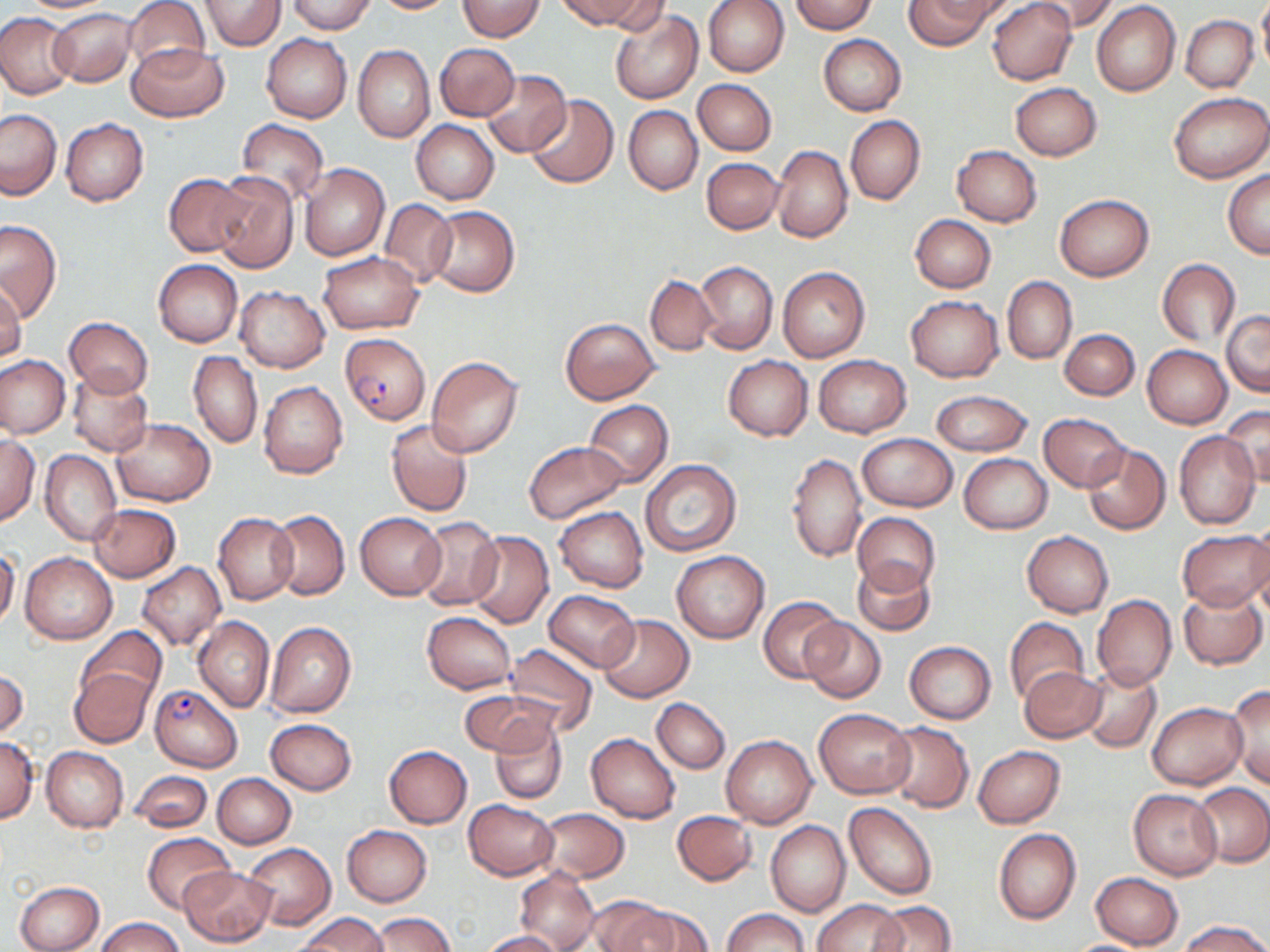

Summary:
  - Coordinate format: approximate bounding boxes as [x1, y1, x2, y2] in pixels
  - Uninfected red blood cell locations: [14, 0, 120, 14], [124, 0, 209, 75], [200, 0, 286, 50], [288, 0, 376, 34], [372, 0, 460, 14], [558, 0, 650, 31], [701, 0, 790, 78], [904, 0, 998, 51], [987, 0, 1077, 85], [1030, 0, 1120, 33], [1257, 0, 1270, 77], [458, 1, 543, 40], [601, 1, 670, 35], [790, 1, 877, 33], [1092, 2, 1181, 97], [51, 8, 136, 86], [609, 8, 704, 105], [0, 13, 76, 98], [1181, 16, 1258, 92], [261, 33, 351, 124], [818, 34, 906, 116], [127, 43, 228, 121], [435, 44, 519, 121], [353, 45, 434, 142], [482, 69, 571, 157], [693, 79, 776, 155], [1010, 82, 1102, 161], [1168, 92, 1269, 183], [527, 94, 618, 189], [624, 105, 702, 195], [0, 109, 62, 198], [845, 115, 925, 206], [60, 119, 148, 206], [235, 119, 329, 205], [411, 121, 499, 204], [772, 144, 852, 243], [951, 146, 1041, 226], [702, 157, 783, 234], [300, 164, 390, 260], [1223, 169, 1270, 258], [211, 171, 300, 274], [164, 174, 252, 257], [1054, 194, 1154, 281], [380, 198, 457, 287], [426, 206, 519, 296], [910, 215, 997, 292], [0, 220, 62, 321], [318, 251, 424, 334], [1157, 259, 1241, 346], [154, 260, 242, 347], [695, 260, 778, 355], [777, 267, 870, 361], [645, 275, 717, 355], [1003, 276, 1077, 364], [0, 285, 26, 362], [234, 286, 331, 372], [907, 296, 1003, 381], [1222, 311, 1270, 396], [64, 318, 153, 399], [560, 318, 660, 404], [1060, 328, 1140, 401], [1142, 345, 1232, 428], [188, 351, 262, 448], [0, 355, 70, 438], [723, 355, 813, 441], [813, 356, 910, 438], [427, 357, 523, 458], [67, 369, 153, 456], [258, 381, 348, 479], [930, 390, 1032, 456], [420, 397, 513, 504], [584, 401, 673, 486], [1220, 406, 1270, 486], [1038, 412, 1129, 491], [111, 418, 215, 507], [385, 418, 475, 517], [1174, 431, 1260, 530], [857, 434, 957, 511], [0, 437, 39, 525], [523, 439, 629, 524], [1081, 443, 1172, 534], [41, 450, 121, 545], [787, 452, 867, 562], [959, 454, 1051, 534], [641, 459, 742, 557], [88, 503, 181, 582], [555, 507, 648, 593], [270, 510, 349, 600], [355, 512, 446, 600], [853, 512, 941, 597], [213, 513, 299, 605], [415, 516, 504, 611], [1249, 517, 1270, 610], [1176, 530, 1269, 612], [466, 531, 554, 629], [1022, 531, 1114, 616], [0, 548, 19, 628], [672, 551, 769, 643], [21, 553, 117, 644], [853, 560, 934, 636], [137, 562, 226, 651], [1178, 587, 1268, 670], [545, 589, 639, 673], [1091, 594, 1177, 690], [760, 596, 843, 683], [422, 612, 515, 693], [599, 614, 694, 701], [193, 617, 274, 712], [800, 617, 886, 703], [1004, 617, 1089, 707], [266, 622, 357, 719], [78, 627, 167, 709], [905, 641, 996, 723], [503, 644, 599, 736], [1080, 663, 1162, 754], [1019, 666, 1107, 743], [69, 668, 154, 748], [0, 670, 28, 739], [1226, 685, 1269, 790], [461, 690, 554, 759], [652, 697, 730, 773], [1147, 701, 1246, 789], [814, 708, 915, 798], [265, 718, 358, 795], [490, 718, 566, 804], [881, 721, 974, 813], [586, 732, 681, 823], [722, 736, 816, 828], [0, 737, 40, 823], [41, 746, 128, 832], [384, 746, 472, 828], [973, 746, 1065, 827], [129, 771, 212, 833], [213, 773, 296, 848], [1192, 783, 1270, 867], [1129, 788, 1222, 880], [464, 799, 557, 879], [846, 803, 938, 900], [532, 807, 628, 883], [671, 810, 758, 886], [766, 821, 850, 918], [342, 824, 432, 906], [994, 829, 1080, 925], [143, 832, 233, 913], [243, 843, 336, 930], [178, 866, 277, 947], [515, 868, 600, 952], [1089, 871, 1185, 949], [14, 879, 104, 952], [584, 896, 673, 952], [814, 899, 906, 952], [869, 901, 957, 952], [611, 903, 710, 952], [723, 909, 807, 952], [373, 912, 453, 952], [299, 913, 388, 952], [95, 916, 184, 952], [1181, 920, 1269, 952], [480, 930, 563, 951], [1058, 938, 1158, 952]
  - Plasmodium falciparum-infected red blood cell locations: [340, 334, 430, 424], [150, 685, 242, 772]
  - Slide-level diagnosis: Plasmodium falciparum
  - Preparation: thin blood smear
  - Magnification: 1000x
  - Stain: May-Grünwald-Giemsa
  - Image size: 1270×952 pixels
  - Modality: light microscopy
  - Field of view: single